Give the extent of all Plasmodium falciparum-infected red blood cells.
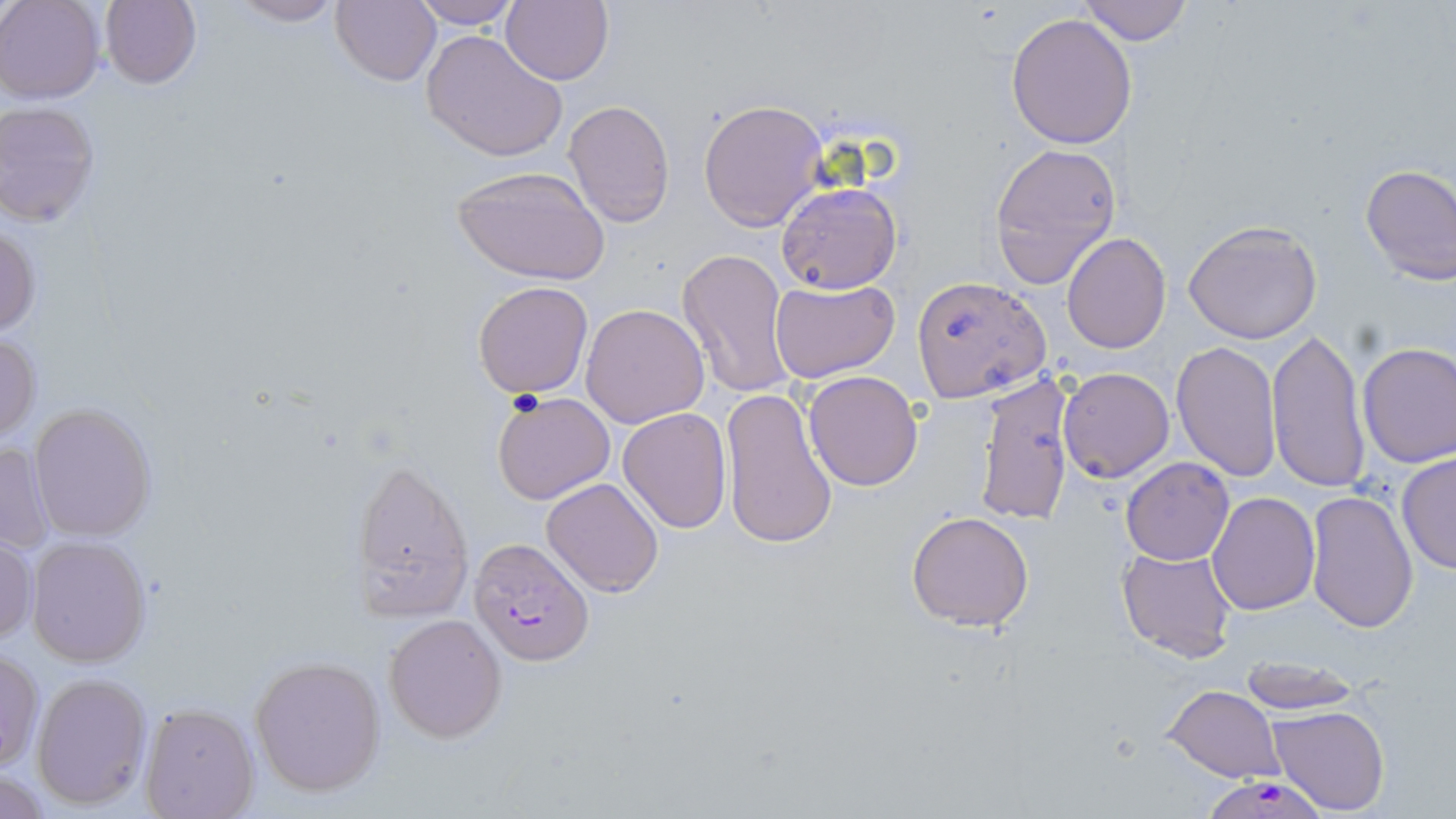
Approximate bounding boxes as [x1, y1, x2, y2] in pixels.
Plasmodium falciparum-infected red blood cells: [468, 538, 595, 666], [1210, 781, 1322, 819].

{
  "slide_level_diagnosis": "Plasmodium falciparum",
  "preparation": "thin blood smear",
  "field_of_view": "single",
  "magnification": "1000x",
  "modality": "light microscopy",
  "uninfected_red_blood_cell_locations": "approximate bounding boxes as [x1, y1, x2, y2] in pixels: [1, 0, 104, 103], [100, 0, 202, 89], [225, 0, 346, 26], [330, 0, 441, 87], [502, 0, 613, 86], [1076, 0, 1196, 46], [403, 1, 526, 29], [1005, 13, 1137, 149], [422, 30, 567, 162], [564, 98, 674, 228], [697, 98, 827, 231], [0, 101, 101, 226], [988, 141, 1122, 290], [1358, 164, 1456, 284], [450, 166, 612, 286], [776, 182, 902, 294], [0, 219, 40, 341], [1184, 219, 1323, 343], [1062, 233, 1170, 352], [677, 247, 796, 401], [912, 276, 1051, 403], [769, 279, 899, 385], [472, 281, 593, 398], [581, 303, 710, 428], [1266, 326, 1370, 495], [0, 331, 41, 445], [1171, 341, 1281, 482], [1357, 341, 1455, 466], [1058, 367, 1174, 482], [803, 370, 924, 491], [973, 373, 1077, 525], [720, 386, 839, 551], [491, 389, 615, 505], [28, 401, 159, 543], [618, 407, 732, 533], [1, 439, 54, 557], [1396, 452, 1455, 576], [1120, 457, 1234, 565], [349, 458, 472, 621], [541, 476, 665, 598], [1305, 491, 1418, 634], [1207, 492, 1319, 614], [905, 510, 1035, 631], [0, 533, 36, 646], [26, 535, 153, 668], [1116, 545, 1237, 664], [383, 614, 507, 741], [0, 649, 43, 770], [249, 655, 386, 796], [1236, 656, 1362, 713], [31, 671, 152, 809], [1162, 685, 1284, 782], [139, 703, 260, 819], [1269, 705, 1392, 815]",
  "stain": "May-Grünwald-Giemsa",
  "image_size": "1456×819 pixels"
}